Classify this cell by malaria status.
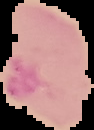

Parasitized.

From a thin blood film. Segmented cell region on a black background. Image is 94×130 pixels.